Evaluate for Plasmodium parasites.
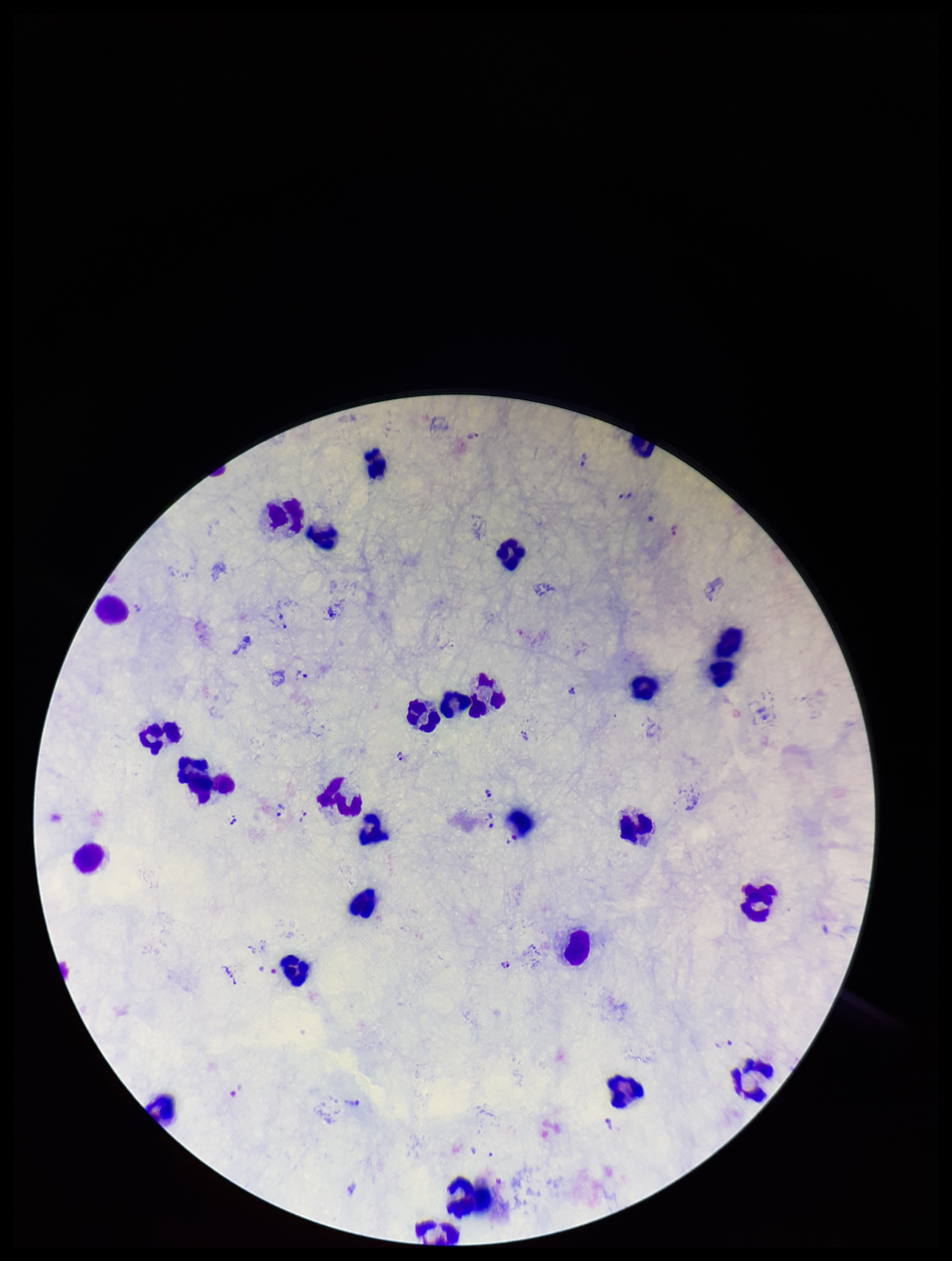

Seen.

Summary:
  - Image size: 952×1261 pixels
  - Leukocyte count: 28
  - Species reported for this patient: Plasmodium vivax
  - Parasite count: 21
  - Stain: Giemsa
  - Field of view: single
  - Capture: smartphone photograph through the microscope eyepiece
  - Patient malaria status: positive
  - Preparation: thick